Assess this cell for malaria.
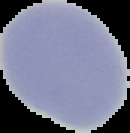
Uninfected.

From a thin blood film. Image is 130×133 pixels. Cell region segmented out of the field of view; the surrounding area is masked to black.